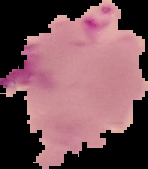

Image is 148×169 pixels. From a thin blood film. Cell region segmented out of the field of view; the surrounding area is masked to black. Result: Plasmodium parasites identified.